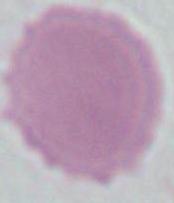

magnification = 1000x
identification = red blood cell
modality = photomicrograph